Classify this cell by malaria status.
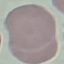
It is uninfected.

Photographed with a smartphone camera at the microscope eyepiece. Thin blood film. Automatically extracted cell patch, resized to 64 × 64 pixels. Giemsa-stained preparation.